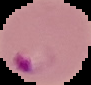
Segmented cell region on a black background. Image is 91×85 pixels. From a thin blood film. Result: malaria parasites identified.